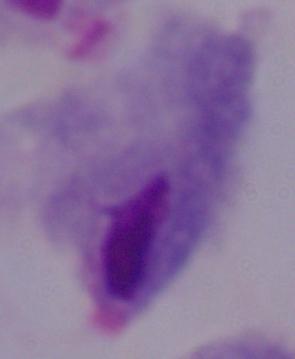
Captured at 1000x magnification. Photomicrograph. A trichomonad is seen.